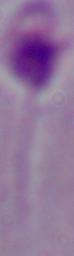
Summary:
  - Modality: micrograph
  - Magnification: 1000x
  - Identification: Leishmania